Outline each blood parasite and name the species.
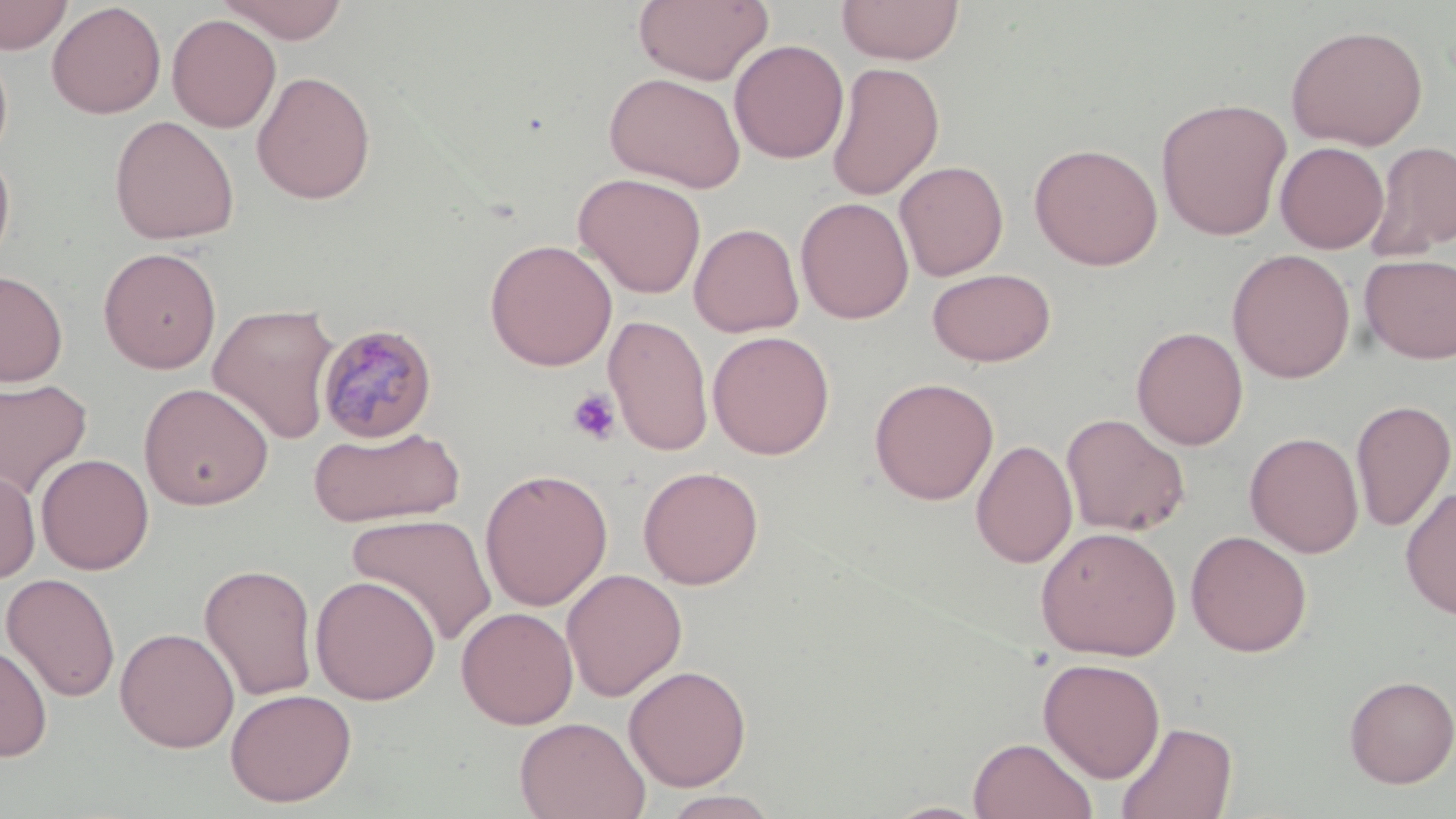

Approximate bounding boxes as (x1,y1)-(x2,y2) corner pairs in pixels.
Plasmodium malariae-infected red blood cells: (316,323)-(439,444).
No Plasmodium falciparum, Plasmodium ovale, Plasmodium vivax, Babesia divergens, or Trypanosoma brucei observed.

Summary:
  - Uninfected red blood cell locations: (1,0)-(73,55), (218,0)-(350,43), (634,0)-(774,86), (836,0)-(965,65), (47,2)-(166,119), (167,14)-(281,133), (1285,24)-(1428,150), (0,39)-(13,169), (729,39)-(849,164), (825,62)-(945,201), (251,70)-(376,204), (604,71)-(747,193), (1155,97)-(1293,240), (109,115)-(240,245), (1368,140)-(1456,260), (1275,141)-(1389,254), (1028,142)-(1163,270), (0,144)-(16,274), (894,160)-(1009,281), (572,172)-(707,299), (795,196)-(914,325), (689,222)-(805,337), (484,238)-(618,371), (98,246)-(222,373), (1227,248)-(1355,383), (1359,253)-(1456,365), (927,268)-(1056,367), (0,269)-(68,387), (208,302)-(340,445), (604,314)-(714,457), (1131,326)-(1249,450), (707,330)-(836,459), (869,377)-(999,505), (0,378)-(93,501), (138,382)-(274,510), (1350,398)-(1456,532), (1060,413)-(1190,537), (307,424)-(465,529), (1245,432)-(1364,558), (971,439)-(1078,569), (36,453)-(155,575), (0,465)-(41,584), (638,465)-(764,589), (479,468)-(613,611), (1400,485)-(1456,621), (347,513)-(497,647), (1034,525)-(1182,661), (1185,530)-(1313,656), (198,562)-(319,702), (561,568)-(687,702), (1,572)-(121,703), (310,575)-(441,705), (456,606)-(578,729), (114,627)-(240,752), (0,642)-(53,762), (1038,657)-(1166,783), (623,663)-(751,792), (1342,674)-(1456,788), (225,688)-(357,807), (514,716)-(650,819), (1115,720)-(1237,819), (967,736)-(1098,819), (660,790)-(781,818), (883,800)-(991,818)
  - Platelet locations: (567,388)-(621,445)
  - Slide-level diagnosis: Plasmodium malariae
  - Field of view: one of a larger specimen
  - Stain: May-Grünwald-Giemsa
  - Magnification: 1000x
  - Image size: 1456×819 pixels
  - Preparation: thin blood smear
  - Modality: optical microscopy